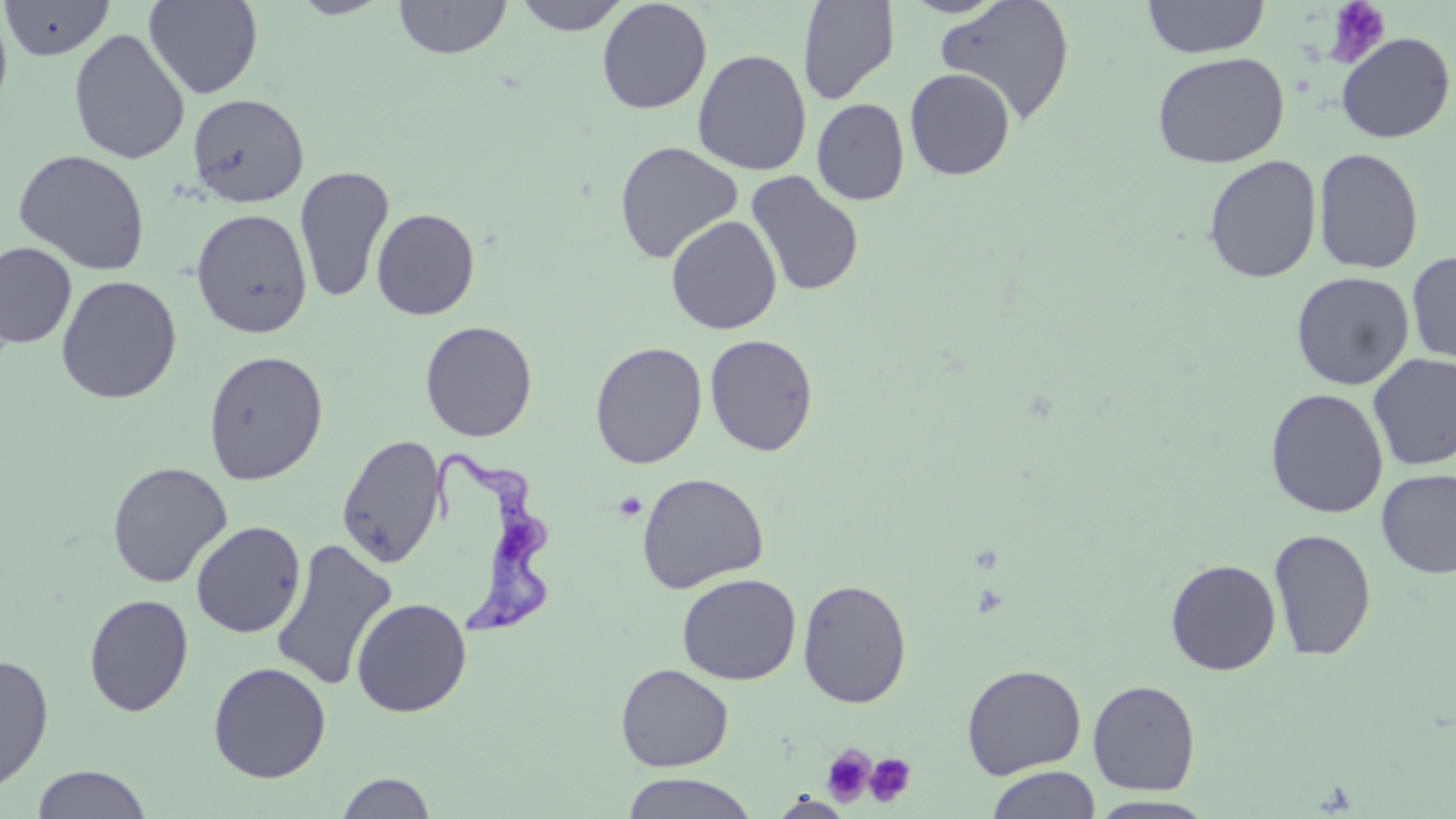 Approximate bounding boxes as [x1, y1, x2, y2] in pixels. Uninfected red blood cell locations: [1, 0, 114, 61], [144, 0, 263, 99], [289, 0, 394, 19], [394, 0, 512, 59], [513, 0, 631, 35], [596, 0, 712, 114], [935, 0, 1076, 125], [1142, 0, 1270, 58], [797, 1, 899, 104], [0, 4, 14, 121], [68, 28, 190, 165], [1335, 31, 1455, 144], [692, 49, 812, 176], [1151, 51, 1289, 168], [904, 68, 1016, 180], [187, 93, 309, 207], [812, 98, 910, 205], [614, 141, 744, 264], [1313, 147, 1424, 274], [13, 148, 151, 275], [1202, 154, 1322, 284], [294, 165, 395, 304], [745, 170, 865, 297], [371, 207, 480, 320], [190, 208, 313, 338], [665, 215, 782, 335], [0, 242, 77, 349], [1406, 250, 1456, 365], [1290, 271, 1415, 390], [55, 275, 182, 404], [420, 320, 538, 442], [704, 333, 819, 456], [590, 341, 707, 468], [202, 349, 329, 485], [1368, 353, 1456, 470], [1265, 388, 1389, 518], [335, 432, 448, 568], [107, 461, 233, 588], [1375, 469, 1456, 579], [637, 472, 770, 594], [191, 520, 307, 638], [1268, 528, 1377, 661], [269, 537, 398, 693], [1165, 558, 1282, 675], [677, 573, 802, 685], [797, 579, 912, 709], [84, 593, 194, 716], [351, 597, 472, 718], [0, 652, 54, 793], [208, 661, 332, 783], [615, 663, 734, 772], [962, 664, 1087, 780], [1087, 679, 1201, 795], [31, 764, 152, 818], [986, 766, 1101, 819], [335, 772, 437, 818], [619, 772, 761, 819], [768, 793, 856, 818], [1087, 796, 1220, 818]. Trypanosoma brucei locations: [432, 445, 556, 635]. Platelet locations: [1323, 1, 1392, 67], [615, 492, 646, 521], [821, 743, 876, 805], [864, 752, 917, 808]. Slide-level diagnosis: Trypanosoma brucei. Optical microscopy. Thin blood film. 1000x magnification. May-Grünwald-Giemsa stain. Image is 1456×819 pixels. Single field of view.